Report the malaria status of this cell.
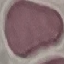

It is uninfected.

Thin blood film. Automatically extracted cell patch, resized to 64 × 64 pixels. Photographed with a smartphone camera at the microscope eyepiece. Giemsa-stained preparation.